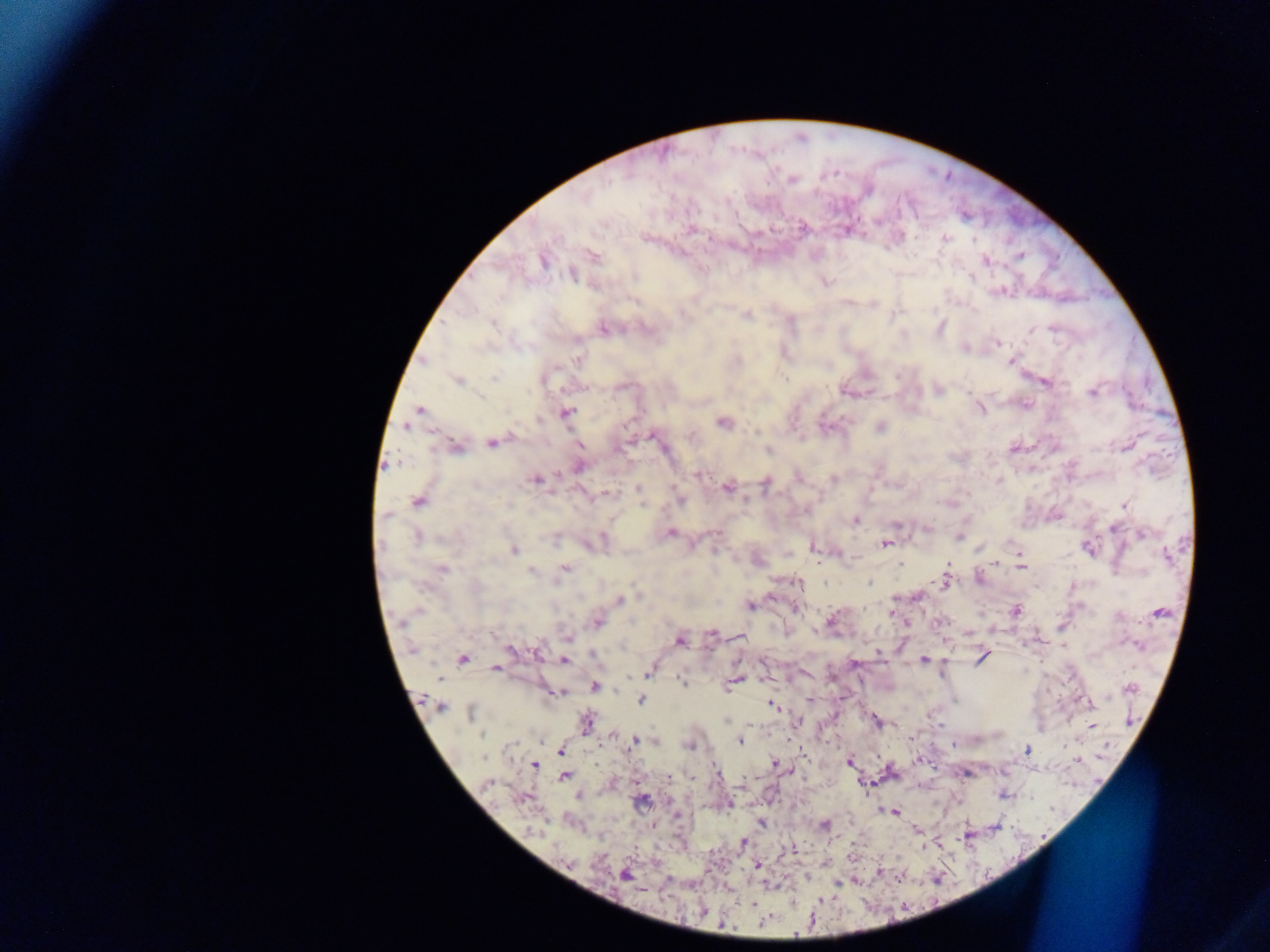
{
  "field_of_view": "single",
  "preparation": "thick blood smear",
  "image_size": "1270×952 pixels",
  "country": "Ghana",
  "plasmodium_parasite_locations": "approximate centers as (x, y) in pixels: (791, 178), (803, 228), (691, 229), (847, 229), (945, 239), (593, 255), (1020, 257), (542, 260), (986, 260), (572, 274), (826, 281), (998, 291), (873, 304), (746, 314), (939, 327), (604, 328), (997, 343), (965, 347), (577, 359), (1011, 360), (458, 380), (1045, 381), (937, 389), (848, 391), (1091, 391), (980, 408), (419, 410), (565, 413), (723, 422), (408, 425), (879, 428), (651, 435), (492, 442), (579, 445), (1127, 445), (454, 446), (1013, 448), (768, 451), (578, 465), (697, 473), (797, 476), (535, 479), (834, 479), (765, 483), (727, 487), (638, 489), (679, 500), (418, 501), (642, 503), (949, 503), (1124, 505), (854, 520), (925, 528), (669, 532), (716, 532), (1141, 534), (416, 536), (958, 536), (596, 541), (884, 543), (812, 546), (1088, 548), (512, 550), (837, 552), (1019, 555), (996, 561), (1020, 566), (442, 569), (563, 569), (531, 570), (978, 578), (945, 581), (798, 583), (917, 596), (619, 600), (749, 605), (796, 607), (1015, 610), (1158, 612), (891, 613), (832, 621), (938, 621), (597, 622), (906, 623), (712, 634), (567, 636), (740, 637), (680, 639), (510, 650), (878, 653), (982, 656), (462, 659), (562, 660), (922, 660), (853, 663), (496, 668), (649, 671), (680, 679), (735, 680), (594, 685), (1130, 687), (556, 692), (641, 699), (809, 700), (1083, 701), (439, 705), (772, 705), (471, 712), (797, 721), (876, 721), (585, 723), (939, 725), (1091, 725), (614, 735), (637, 739), (738, 740), (655, 741), (788, 742), (689, 744), (560, 750), (1027, 750), (919, 759), (1076, 759), (849, 761), (534, 764), (596, 764), (774, 764), (790, 771), (716, 773), (565, 775), (668, 778), (637, 780), (487, 783), (578, 795), (1005, 795), (522, 798), (640, 801), (729, 804), (893, 812), (760, 823), (824, 825), (917, 830), (741, 843), (792, 851), (851, 856), (757, 865), (879, 871), (624, 874), (805, 876), (751, 904), (702, 910)",
  "capture": "mobile-phone photograph through a microscope"
}